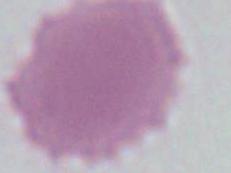
{
  "modality": "photomicrograph",
  "identification": "red blood cell",
  "magnification": "1000x"
}